Give the location of every parasitized RBC.
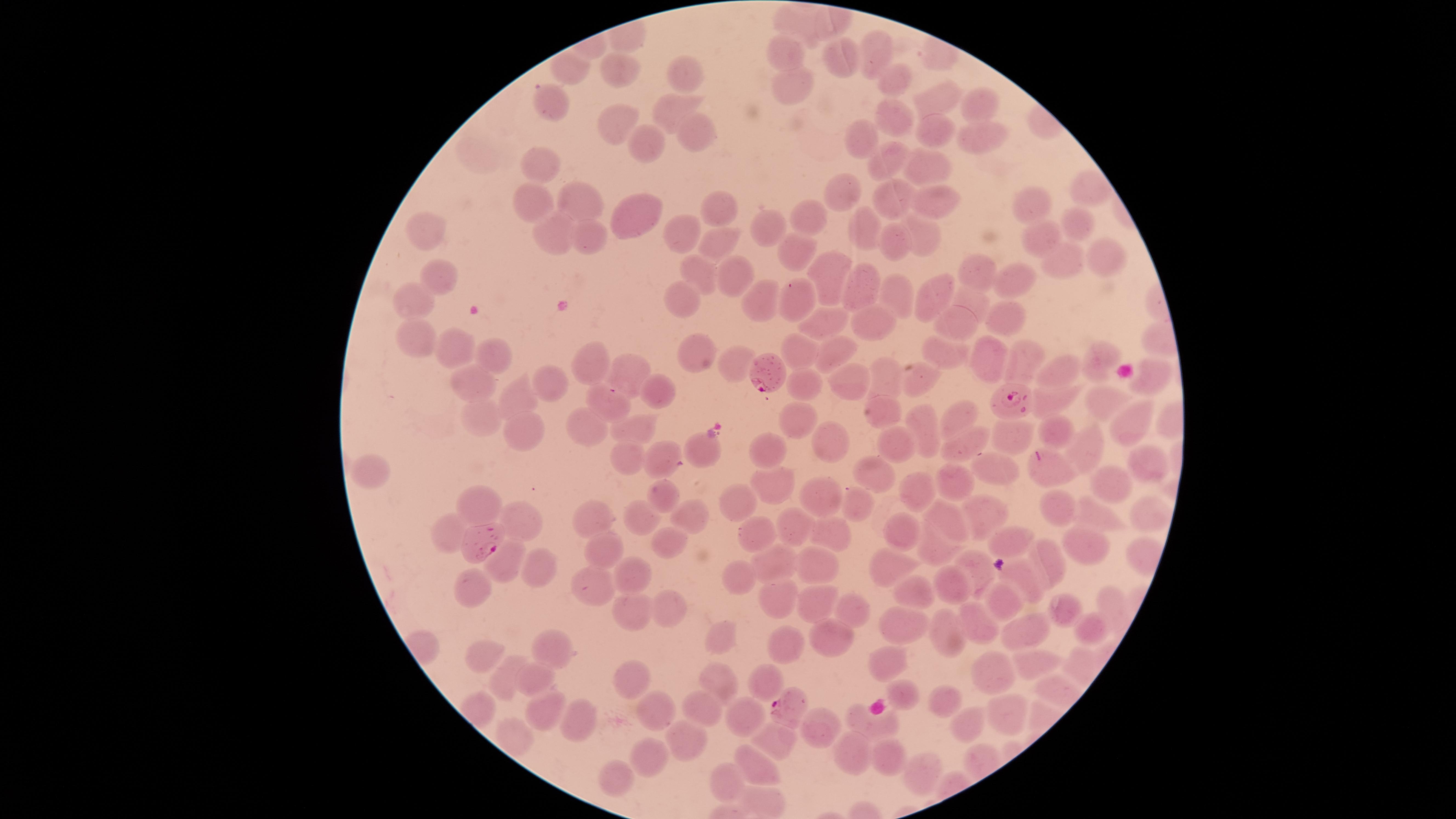

Approximate marker points as {x, y} in pixels.
Parasitized RBCs: {775, 375}, {1013, 404}, {479, 536}, {788, 706}.

stain: Giemsa
species: Plasmodium falciparum
visible_region: circular
capture: smartphone photograph through the microscope eyepiece
image_size: 1456×819 pixels
uninfected_RBCs: 'approximate marker points as {x, y} in pixels: {796, 20}, {783, 51}, {871, 55}, {840, 58}, {577, 71}, {684, 71}, {614, 73}, {895, 81}, {788, 86}, {933, 97}, {546, 102}, {977, 105}, {674, 111}, {895, 118}, {612, 125}, {931, 133}, {694, 134}, {980, 140}, {862, 142}, {647, 143}, {885, 157}, {535, 163}, {927, 166}, {1086, 190}, {843, 194}, {581, 202}, {898, 202}, {938, 202}, {532, 203}, {1033, 203}, {712, 207}, {632, 215}, {810, 217}, {1073, 223}, {866, 225}, {768, 228}, {426, 230}, {587, 234}, {681, 236}, {557, 238}, {928, 238}, {1051, 239}, {895, 248}, {718, 249}, {1106, 249}, {795, 250}, {1063, 262}, {975, 270}, {731, 271}, {700, 273}, {830, 276}, {441, 280}, {1014, 281}, {858, 287}, {934, 295}, {759, 296}, {897, 296}, {681, 301}, {796, 301}, {410, 302}, {969, 302}, {1010, 317}, {871, 321}, {957, 322}, {826, 323}, {416, 342}, {690, 347}, {452, 349}, {799, 352}, {948, 353}, {842, 354}, {1102, 357}, {493, 358}, {984, 358}, {1026, 360}, {594, 362}, {734, 366}, {1057, 371}, {885, 374}, {629, 376}, {1153, 376}, {853, 379}, {918, 382}, {797, 385}, {471, 386}, {550, 386}, {662, 394}, {520, 398}, {1107, 399}, {605, 400}, {1054, 400}, {890, 409}, {959, 415}, {481, 416}, {791, 421}, {1129, 423}, {584, 424}, {924, 424}, {1054, 426}, {646, 427}, {530, 430}, {1010, 436}, {824, 441}, {899, 445}, {965, 445}, {707, 450}, {1087, 450}, {768, 451}, {625, 454}, {661, 461}, {1139, 463}, {869, 470}, {1048, 470}, {366, 472}, {988, 472}, {1108, 483}, {769, 484}, {955, 489}, {918, 493}, {817, 495}, {665, 497}, {745, 504}, {1054, 505}, {858, 507}, {484, 508}, {681, 512}, {982, 514}, {596, 515}, {1140, 515}, {633, 516}, {948, 516}, {1091, 519}, {522, 522}, {795, 527}, {445, 528}, {904, 532}, {751, 533}, {831, 534}, {671, 540}, {1006, 541}, {600, 543}, {1078, 546}, {935, 550}, {1043, 562}, {892, 563}, {819, 564}, {776, 566}, {507, 567}, {535, 570}, {979, 570}, {638, 575}, {1021, 576}, {737, 577}, {595, 584}, {946, 584}, {479, 591}, {915, 598}, {1010, 599}, {779, 600}, {814, 602}, {1111, 603}, {852, 606}, {668, 608}, {1067, 612}, {629, 617}, {902, 623}, {978, 623}, {1023, 624}, {945, 632}, {1089, 632}, {827, 636}, {718, 637}, {787, 643}, {554, 650}, {491, 659}, {884, 661}, {1035, 665}, {996, 673}, {509, 676}, {632, 680}, {535, 681}, {716, 681}, {766, 684}, {906, 691}, {948, 701}, {656, 706}, {703, 708}, {1002, 710}, {548, 711}, {740, 717}, {577, 726}, {819, 727}, {973, 727}, {880, 729}, {683, 738}, {771, 743}, {654, 753}, {850, 757}, {888, 759}, {754, 768}, {923, 773}, {617, 778}, {730, 782}'
field_of_view: single
preparation: thin smear of blood